Classify this cell by malaria status.
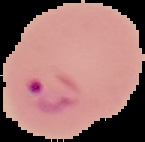

Parasitized.

Summary:
  - Image size: 145×142 pixels
  - Preparation: thin blood film
  - Image type: cell region segmented out of the field of view; surrounding area masked to black